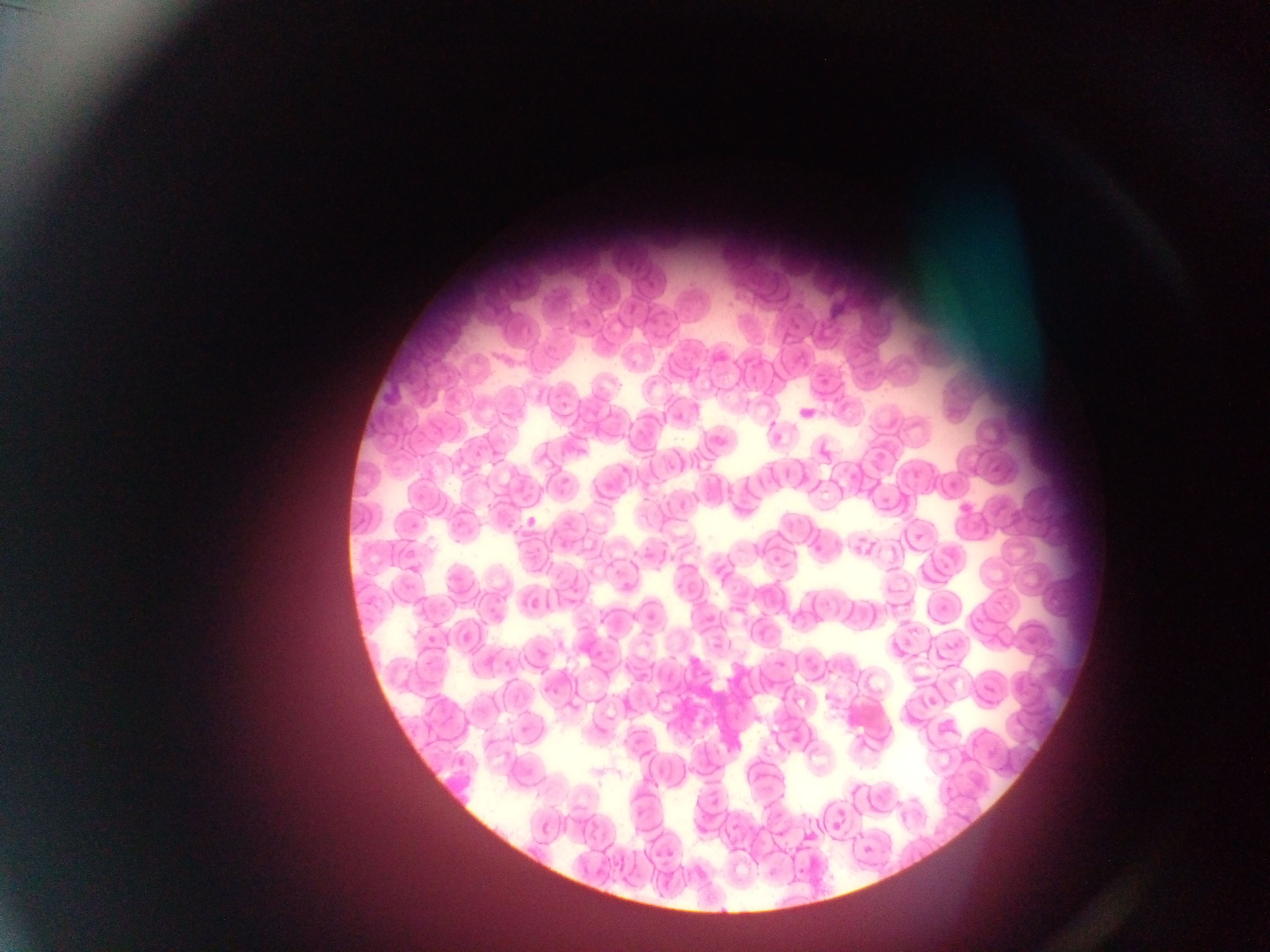
Approximate bounding boxes as [left, top, right, bottom] in pixels.
Summary:
  - Plasmodium parasite locations: [796, 405, 820, 421], [954, 495, 981, 515], [524, 513, 537, 530], [401, 548, 420, 563], [426, 635, 439, 648], [927, 691, 943, 706]
  - Image size: 1270×952 pixels
  - Field of view: single
  - Capture: mobile-phone photograph through a microscope
  - Preparation: thin blood film
  - Country: Ghana